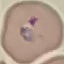 Result: malaria parasites detected. Photographed with a smartphone camera at the microscope eyepiece. Giemsa-stained preparation. Cell patch, automatically extracted from a larger field of view and resized to 64 × 64 pixels. Thin blood film.